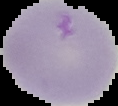 Cell region segmented out of the field of view; the surrounding area is masked to black. Malaria status: uninfected. Image is 118×106 pixels. From a thin blood film.